State which cell type is depicted.
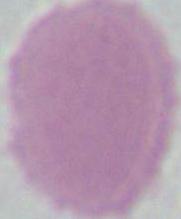
This is an erythrocyte.

Photomicrograph. 1000x magnification.